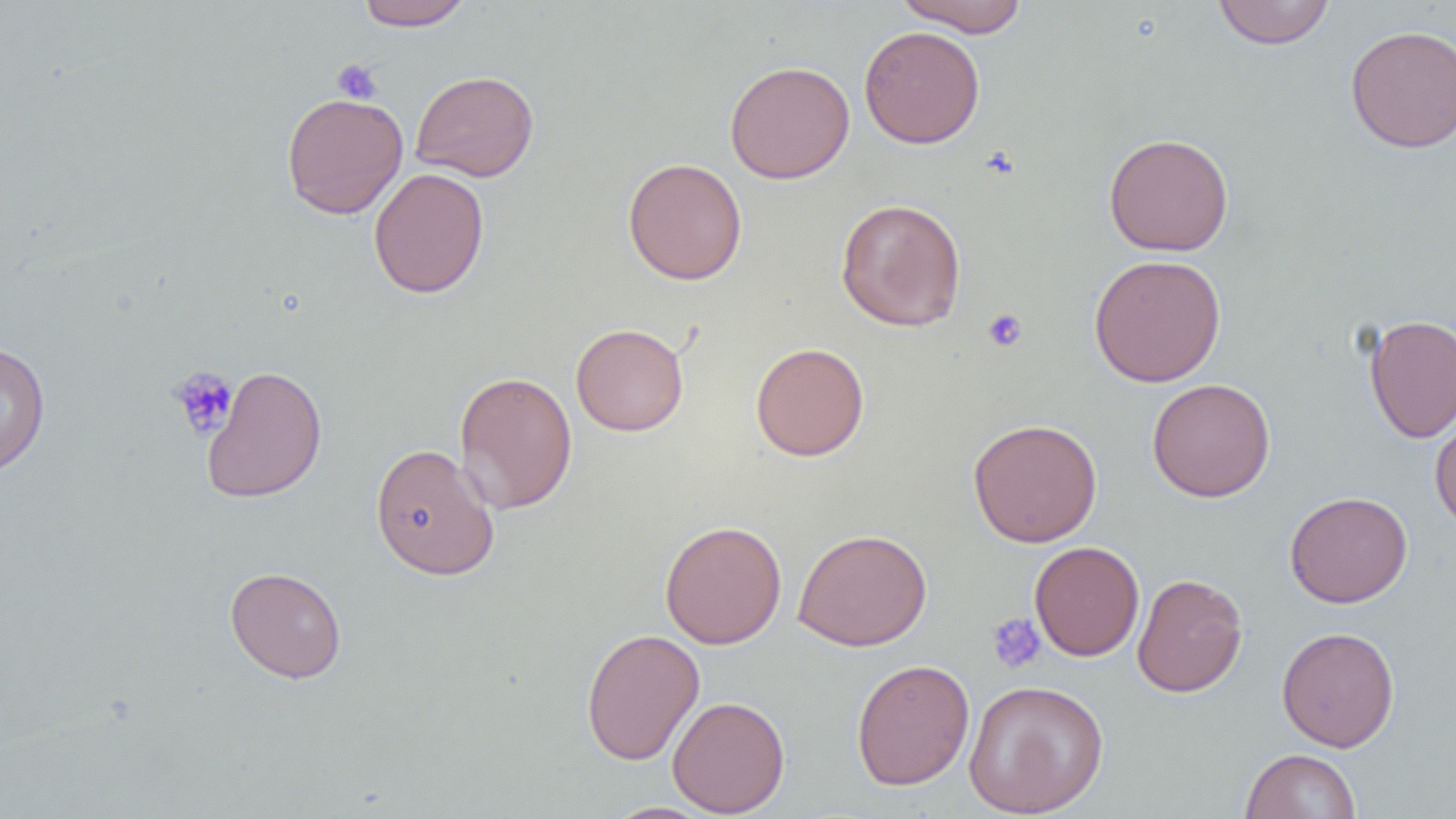

Approximate bounding boxes as [x1, y1, x2, y2] in pixels. Platelet locations: [331, 59, 382, 105], [982, 308, 1028, 352], [169, 367, 237, 440], [987, 612, 1046, 674]. Uninfected red blood cell locations: [895, 0, 1031, 36], [355, 1, 475, 31], [1212, 1, 1335, 49], [1345, 24, 1456, 153], [859, 25, 985, 149], [724, 60, 855, 183], [411, 70, 539, 182], [281, 92, 408, 219], [1103, 132, 1234, 256], [622, 157, 747, 285], [368, 167, 489, 298], [835, 198, 966, 332], [1088, 254, 1226, 388], [1364, 313, 1456, 443], [570, 322, 689, 436], [0, 341, 51, 479], [751, 342, 869, 461], [201, 364, 327, 502], [453, 370, 578, 514], [1147, 378, 1276, 502], [1429, 409, 1456, 533], [968, 418, 1102, 547], [370, 443, 499, 581], [1284, 490, 1413, 608], [659, 520, 787, 649], [793, 528, 932, 652], [1029, 541, 1144, 661], [225, 566, 347, 684], [1132, 573, 1249, 698], [1276, 625, 1400, 752], [580, 627, 704, 765], [851, 659, 975, 790], [963, 680, 1109, 817], [667, 696, 790, 817], [1240, 748, 1361, 819], [600, 802, 718, 819]. Slide-level diagnosis: no evidence of blood parasites. Single field of view. Image is 1456×819 pixels. Thin blood film. 1000x magnification. Light microscopy.